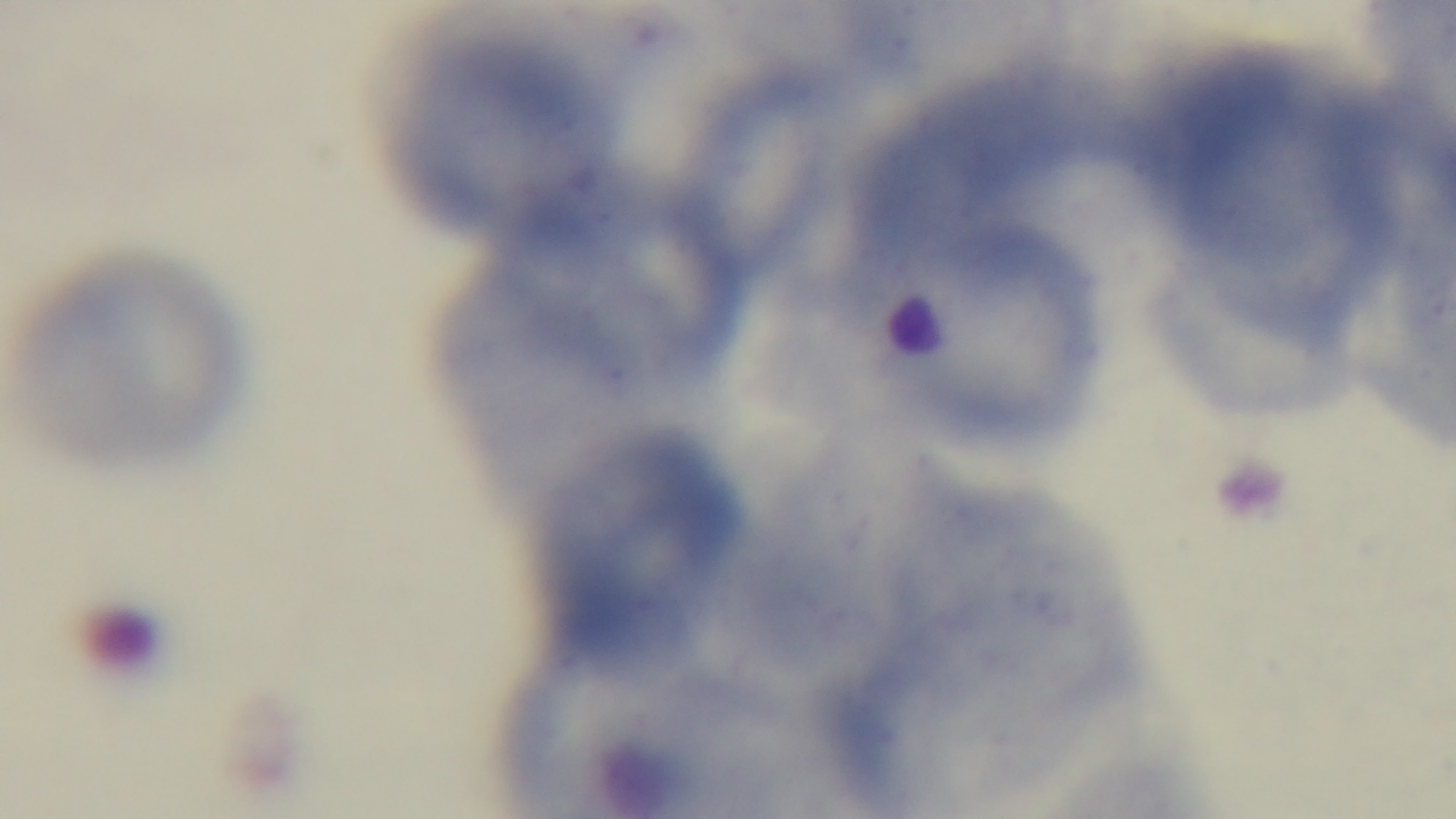 100x oil-immersion objective. Preparation: thin. Mounted 4K digital camera. Light microscopy. Giemsa stain. One field from the slide. Malaria status: uninfected.